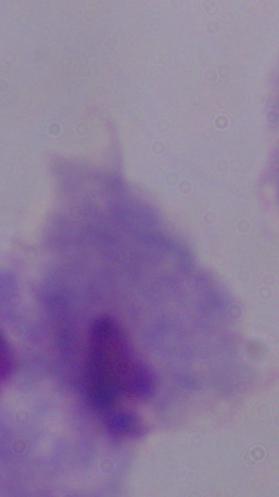
modality: photomicrograph
identification: trichomonad
magnification: 1000x